Assess this cell for malaria.
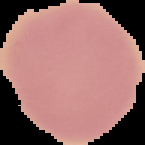

It is uninfected.

Image is 145×145 pixels. Segmented cell region on a black background. From a thin blood smear.